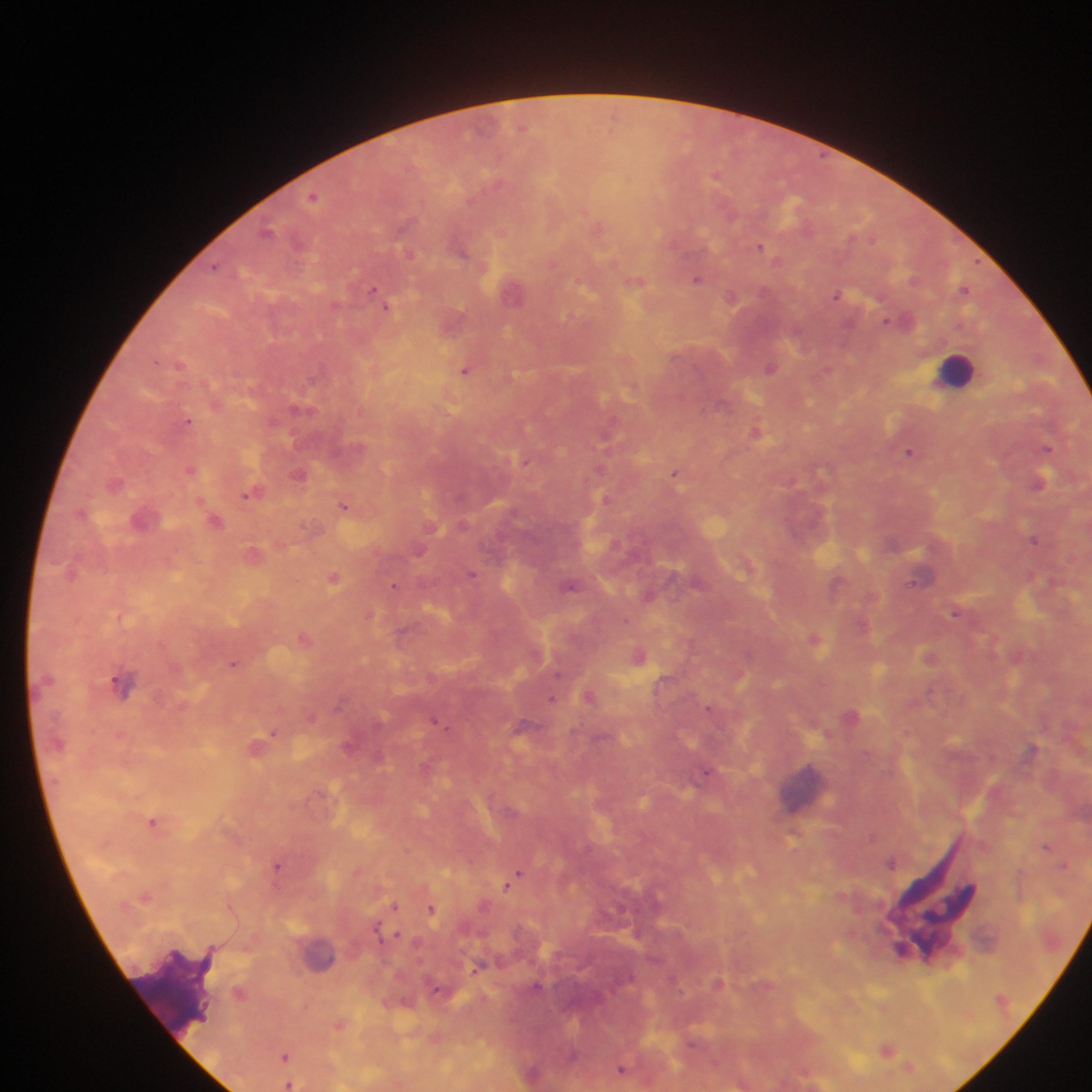

malaria parasite locations = approximate centers as (x, y) in pixels: (522, 127), (313, 196), (598, 226), (267, 231), (759, 247), (462, 252), (409, 254), (216, 266), (697, 279), (635, 281), (373, 289), (964, 290), (512, 291), (837, 294), (731, 296), (386, 305), (888, 320), (179, 364), (771, 368), (465, 370), (297, 408), (189, 421), (754, 432), (605, 435), (1048, 449), (909, 452), (526, 462), (190, 469), (599, 469), (675, 473), (298, 474), (1039, 481), (247, 495), (605, 497), (344, 506), (214, 522), (1034, 540), (419, 550), (471, 574), (919, 576), (333, 577), (393, 585), (571, 586), (835, 587), (955, 612), (369, 616), (402, 630), (304, 639), (814, 639), (639, 656), (928, 657), (233, 664), (558, 673), (122, 684), (589, 696), (552, 699), (709, 708), (435, 721), (273, 732), (1033, 749), (708, 772), (152, 822), (792, 837), (873, 837), (1045, 846), (892, 862), (1062, 865), (277, 866), (517, 875), (507, 885), (394, 906), (430, 909), (376, 929), (396, 934), (480, 965), (536, 986), (240, 993), (887, 1049), (572, 1055), (285, 1056), (908, 1067), (621, 1068), (289, 1085)
country = Ghana
image size = 1092×1092 pixels
field of view = single
preparation = thick blood smear
leukocyte locations = approximate centers as (x, y) in pixels: (956, 370), (801, 793), (321, 954)
capture = mobile-phone photograph through a microscope